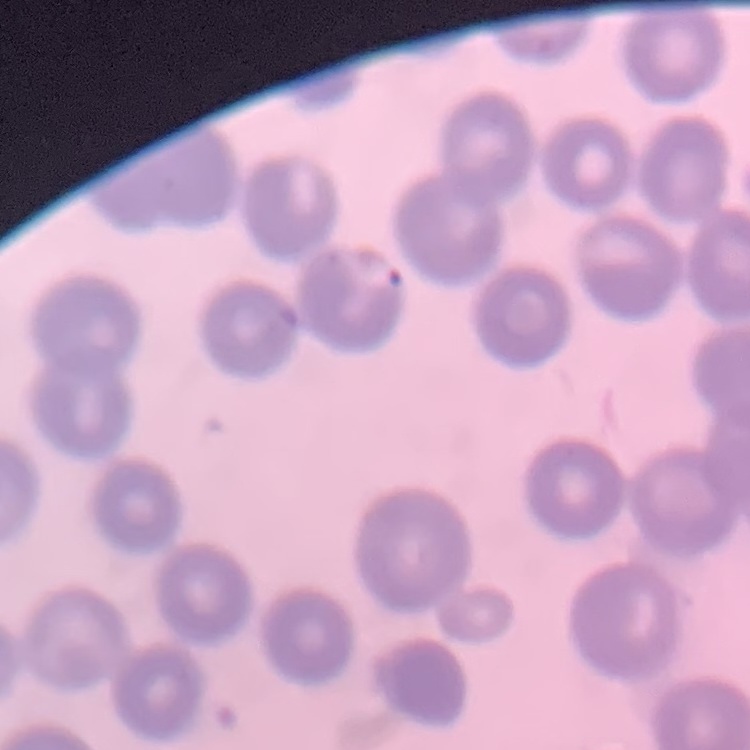
red_blood_cell_morphology: no rouleaux formation
image_type: one tile cut from a larger photomicrograph
stain: Field's or Giemsa
preparation: thin peripheral smear